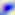

identification = Toxoplasma gondii
modality = micrograph
magnification = 400x